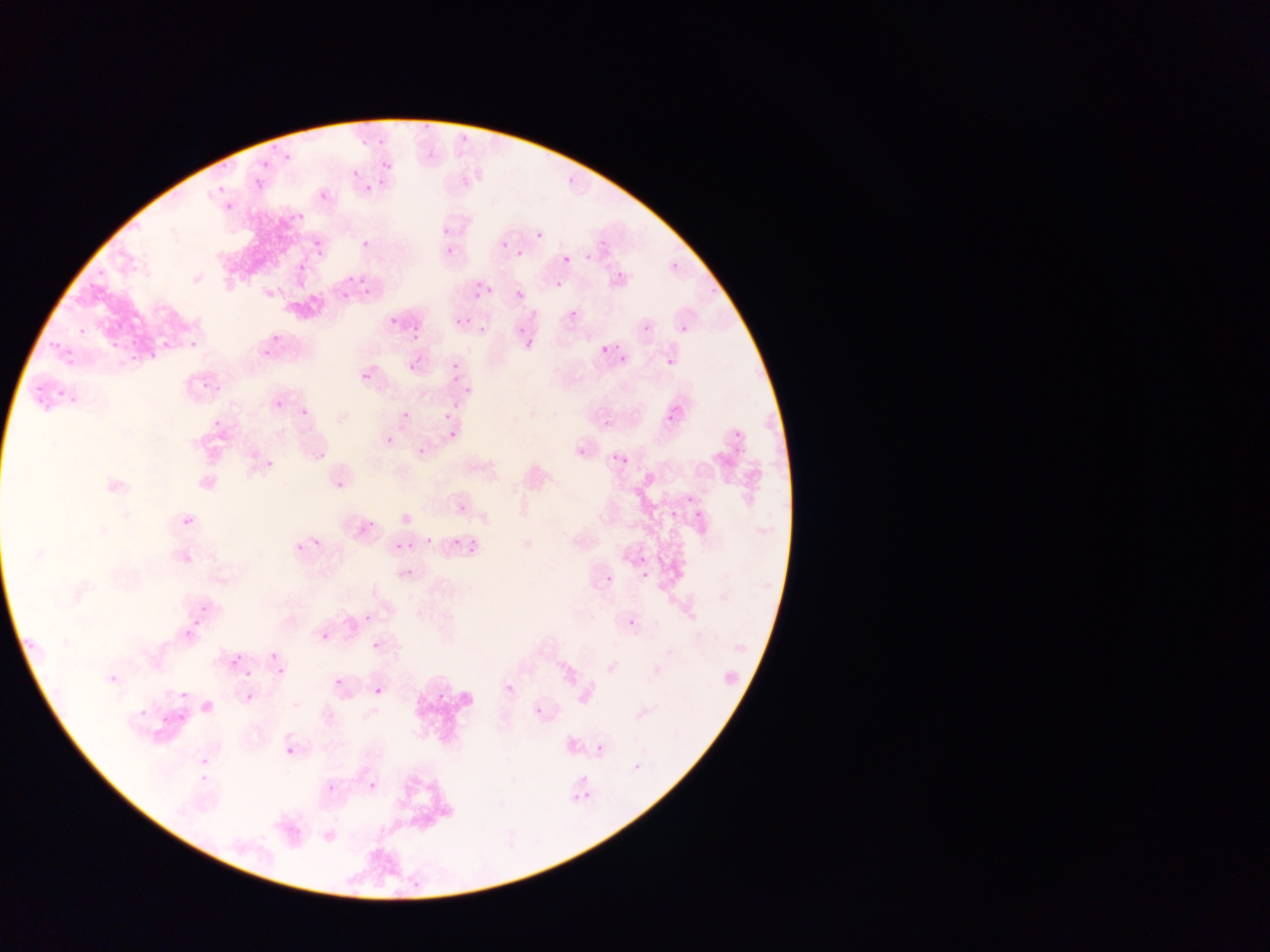

Approximate bounding boxes as (left, top, right, bottom) in pixels. Malaria parasite locations: (419, 123, 436, 134), (373, 134, 392, 144), (359, 136, 372, 150), (457, 136, 467, 147), (269, 143, 276, 152), (280, 152, 294, 169), (381, 152, 389, 178), (217, 159, 236, 172), (259, 160, 272, 170), (350, 167, 367, 177), (253, 176, 266, 191), (563, 177, 576, 187), (217, 181, 225, 195), (360, 182, 382, 195), (319, 190, 329, 201), (222, 201, 239, 213), (297, 207, 308, 221), (286, 215, 295, 227), (443, 228, 450, 236), (534, 228, 552, 246), (359, 235, 376, 249), (313, 238, 325, 249), (442, 241, 455, 254), (499, 241, 506, 249), (511, 246, 527, 258), (582, 249, 594, 262), (563, 255, 572, 263), (298, 262, 307, 272), (671, 262, 679, 270), (95, 264, 105, 279), (612, 271, 624, 278), (347, 274, 366, 284), (84, 280, 97, 291), (471, 281, 482, 288), (556, 281, 564, 289), (362, 284, 375, 296), (703, 286, 720, 299), (483, 287, 491, 295), (473, 288, 482, 301), (339, 291, 351, 300), (514, 291, 523, 301), (569, 305, 584, 320), (387, 315, 402, 326), (463, 316, 474, 326), (679, 317, 696, 333), (455, 318, 464, 326), (410, 322, 423, 342), (265, 323, 291, 347), (76, 324, 88, 337), (475, 325, 488, 334), (515, 326, 523, 334), (639, 326, 653, 336), (47, 335, 61, 350), (127, 336, 137, 350), (156, 336, 170, 351), (185, 336, 200, 351), (516, 336, 534, 352), (110, 338, 123, 354), (611, 342, 622, 356), (259, 343, 274, 357), (600, 345, 610, 355), (147, 347, 159, 365), (126, 351, 138, 362), (66, 352, 83, 366), (407, 352, 431, 371), (619, 355, 627, 363), (448, 359, 461, 370), (665, 359, 678, 371), (448, 372, 467, 387), (362, 373, 370, 382), (200, 375, 212, 393), (31, 377, 47, 402), (214, 378, 227, 397), (460, 385, 473, 404), (57, 386, 64, 403), (68, 392, 77, 409), (294, 397, 312, 419), (450, 397, 458, 411), (42, 401, 53, 413), (275, 401, 284, 410), (441, 409, 454, 423), (402, 410, 410, 419), (663, 415, 677, 425), (212, 418, 221, 427), (605, 420, 613, 429), (725, 426, 743, 441), (448, 430, 456, 438), (384, 435, 394, 444), (313, 444, 327, 461), (417, 447, 426, 455), (576, 447, 587, 461), (610, 455, 621, 464), (619, 457, 633, 467), (267, 460, 274, 468), (337, 473, 344, 486), (683, 498, 694, 506), (458, 505, 467, 514), (669, 511, 677, 522), (694, 513, 701, 523), (360, 516, 381, 535), (183, 517, 192, 525), (309, 530, 328, 547), (406, 537, 413, 550), (422, 537, 431, 546), (451, 538, 459, 546), (464, 538, 481, 551), (290, 539, 310, 561), (395, 543, 404, 551), (635, 556, 647, 565), (400, 568, 410, 578), (640, 571, 648, 579), (606, 575, 613, 584), (199, 601, 212, 617), (356, 613, 374, 627), (628, 619, 636, 628), (194, 621, 205, 633), (183, 630, 193, 639), (321, 633, 330, 642), (370, 635, 382, 649), (22, 638, 38, 653), (266, 653, 278, 664), (230, 657, 240, 667), (276, 666, 284, 675), (245, 669, 252, 678), (107, 674, 119, 684), (334, 678, 343, 687), (506, 684, 514, 693), (374, 688, 382, 696), (436, 688, 450, 705), (180, 692, 189, 700), (241, 692, 259, 706), (136, 703, 149, 715), (535, 707, 543, 716), (177, 709, 190, 729), (159, 715, 173, 726), (596, 745, 603, 753), (286, 746, 294, 754), (629, 756, 652, 777), (197, 770, 212, 787), (326, 777, 343, 798), (369, 782, 377, 790), (580, 785, 593, 801), (570, 793, 584, 805) | approximate (x, y) pixel centers of objects too small to bound: (204, 761). Sample from Ghana. Image is 1270×952 pixels. Photographed through a microscope with a mobile-phone camera. One field of view. Thin blood smear.